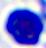
Summary:
  - Modality: micrograph
  - Magnification: 400x
  - Identification: leukocyte